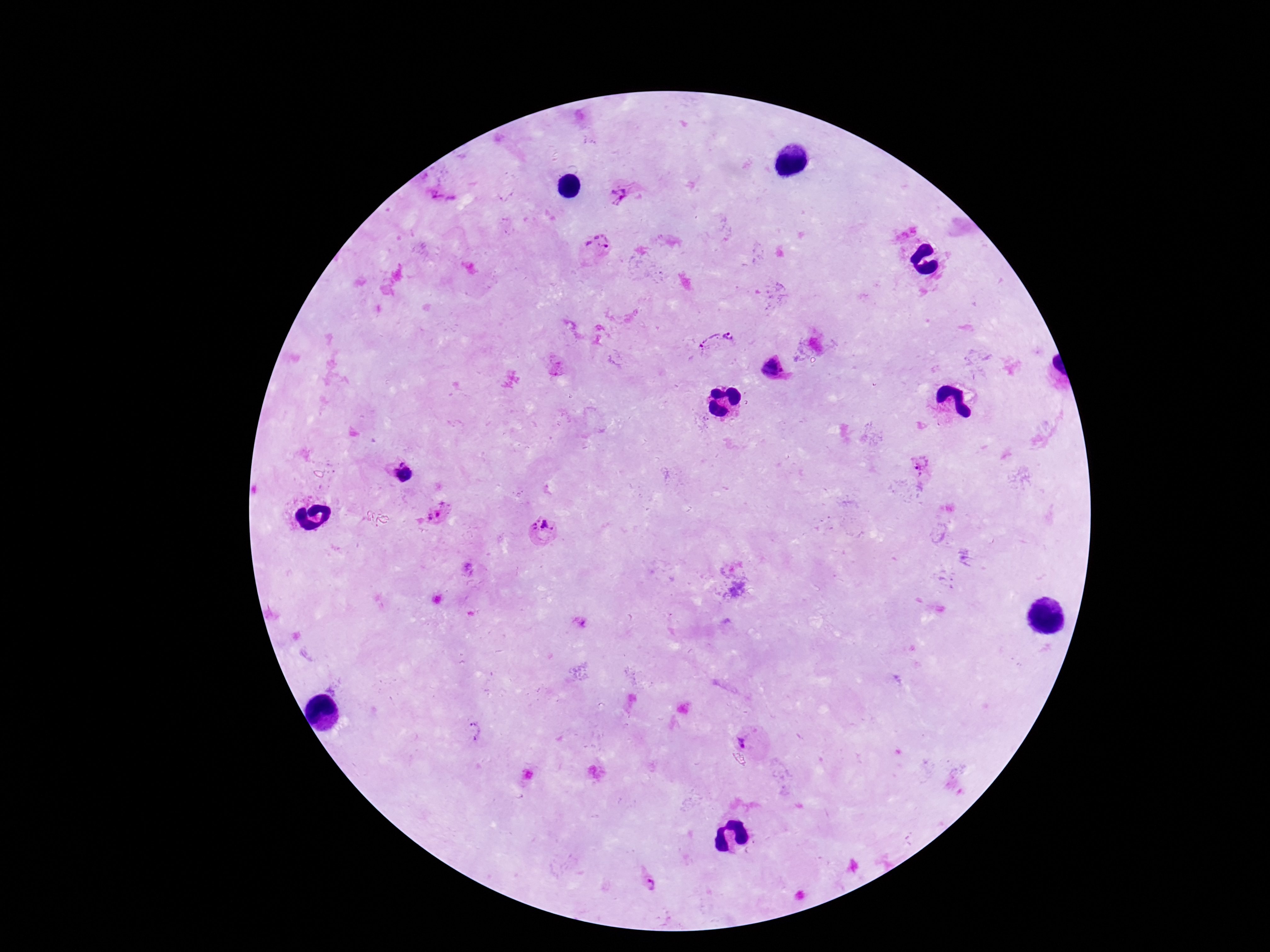

stain: Giemsa
field_of_view: one from this slide
patient_malaria_status: positive
magnification: 100x
plasmodium_parasite_locations: 'approximate object centers, in pixels from the top-left corner: (x=623, y=195), (x=445, y=198), (x=597, y=248), (x=729, y=337), (x=707, y=342), (x=772, y=370), (x=921, y=465), (x=401, y=473), (x=438, y=515), (x=541, y=530), (x=580, y=622), (x=474, y=731), (x=747, y=740)'
image_size: 1270×952 pixels
preparation: thick blood film
capture: smartphone camera through the microscope eyepiece